Classify this cell by malaria status.
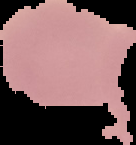

It is uninfected.

image size = 136×145 pixels
preparation = thin blood film
image type = cell region segmented out of the field of view; surrounding area masked to black